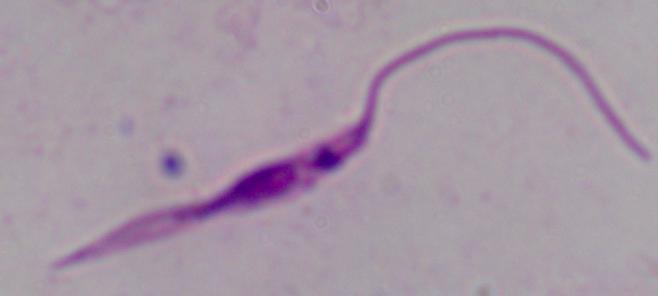 Micrograph. A Leishmania parasite is shown. Captured at 1000x magnification.